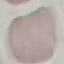

malaria_status: uninfected
stain: Giemsa
preparation: thin blood smear
image_type: automatically extracted cell patch, resized to 64 × 64 pixels
capture: smartphone through the microscope eyepiece